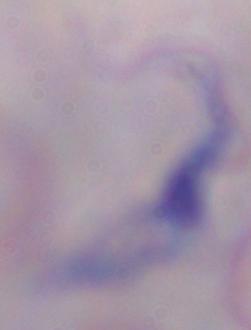

A trypanosome is shown. Micrograph. Captured at 1000x magnification.